Identify the parasite.
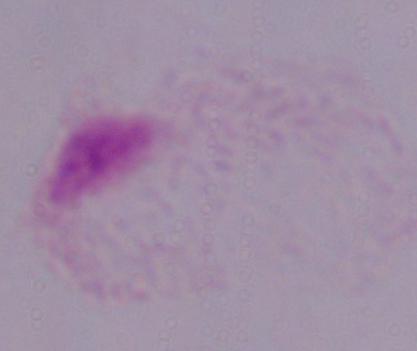

A trichomonad.

Captured at 1000x magnification. Photomicrograph.